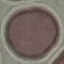
result = no malaria parasites detected
preparation = thin blood film
stain = Giemsa
image type = cell patch, automatically extracted from a larger field of view and resized to 64 × 64 pixels
capture = smartphone camera at the microscope eyepiece